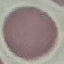

result = negative for malaria parasites
preparation = thin blood film
capture = smartphone through the microscope eyepiece
image type = automatically extracted cell patch, resized to 64 × 64 pixels
stain = Giemsa